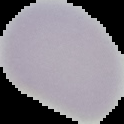
{
  "preparation": "thin blood film",
  "image_type": "cell region segmented out of the field of view; surrounding area masked to black",
  "malaria_status": "uninfected",
  "image_size": "124×124 pixels"
}